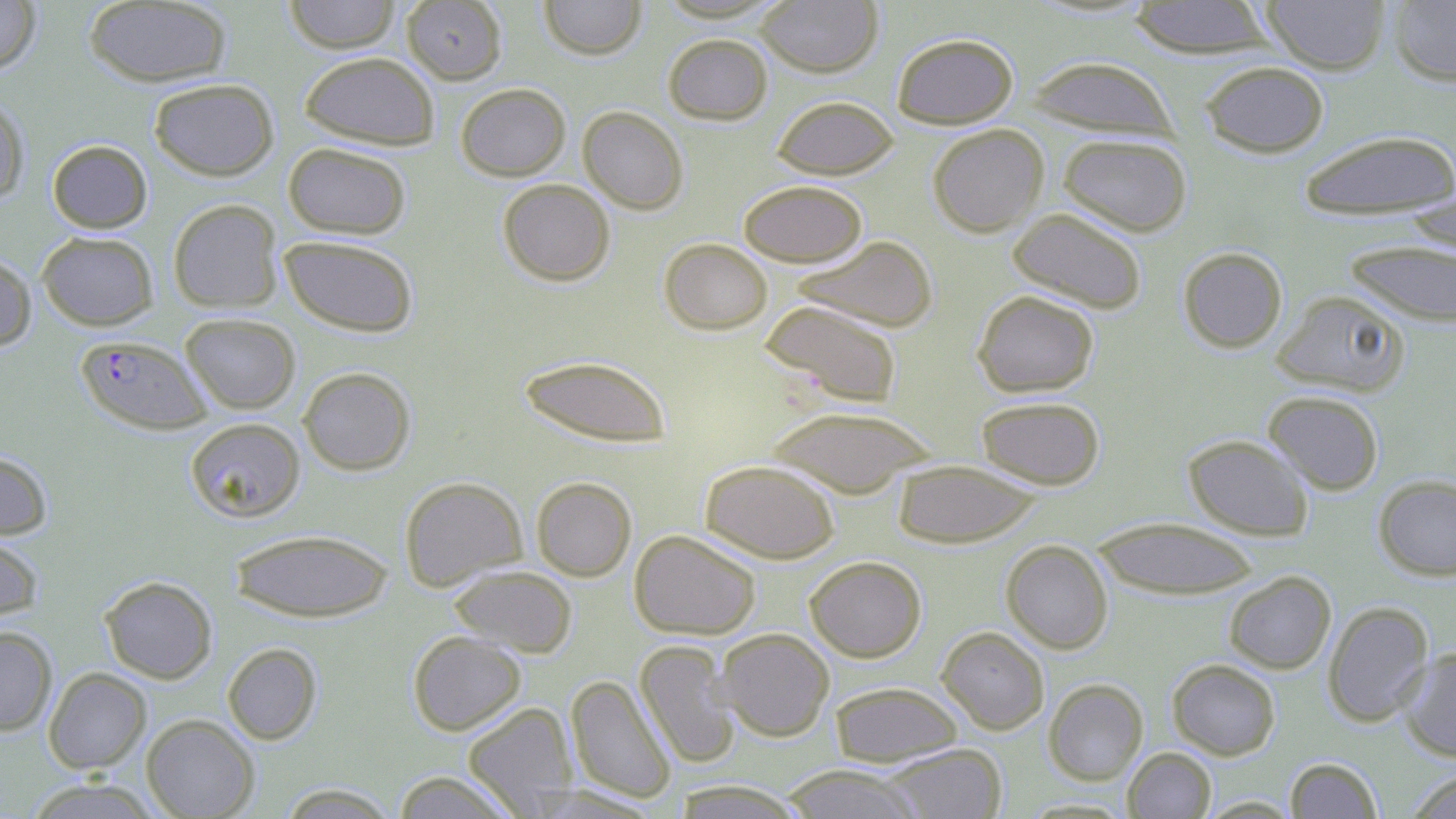
slide-level diagnosis = Plasmodium falciparum
stain = May-Grünwald-Giemsa
image size = 1456×819 pixels
field of view = single
preparation = thin blood film
uninfected red blood cell locations = approximate bounding boxes as (x1,y1)-(x2,y2) corner pairs in pixels: (283,0)-(401,52), (402,0)-(507,84), (539,0)-(646,60), (755,0)-(883,77), (1260,0)-(1391,74), (0,1)-(41,75), (84,1)-(232,88), (1127,1)-(1278,59), (1387,1)-(1456,87), (891,32)-(1018,129), (662,33)-(773,125), (299,51)-(440,150), (1025,55)-(1179,140), (1199,60)-(1330,158), (148,78)-(279,180), (455,82)-(571,181), (771,95)-(899,179), (0,96)-(30,206), (578,106)-(689,214), (927,124)-(1049,237), (1298,130)-(1456,219), (1057,133)-(1193,236), (47,140)-(152,233), (283,142)-(411,239), (497,179)-(615,286), (738,180)-(867,267), (1402,193)-(1455,257), (167,199)-(283,313), (1008,207)-(1148,314), (37,231)-(159,330), (279,235)-(419,337), (791,235)-(939,333), (659,238)-(773,335), (1344,240)-(1456,328), (1177,246)-(1288,353), (0,254)-(37,351), (972,289)-(1100,397), (1272,289)-(1410,397), (759,300)-(904,408), (180,313)-(301,414), (517,354)-(673,448), (298,366)-(416,475), (1262,390)-(1385,494), (975,395)-(1106,490), (763,405)-(939,498), (185,417)-(306,522), (1182,434)-(1314,540), (0,450)-(53,539), (700,459)-(841,563), (892,459)-(1043,548), (1373,474)-(1456,581), (399,476)-(528,592), (531,476)-(636,581), (1090,516)-(1261,599), (228,528)-(394,622), (629,529)-(761,640), (0,532)-(45,624), (1001,539)-(1114,654), (804,556)-(926,662), (449,565)-(577,657), (1224,570)-(1336,674), (99,575)-(217,684), (1322,601)-(1435,726), (0,626)-(58,736), (936,626)-(1050,735), (715,628)-(835,741), (408,630)-(526,735), (634,640)-(741,769), (222,642)-(322,744), (1397,648)-(1456,761), (1167,659)-(1280,760), (43,667)-(151,774), (565,674)-(676,804), (1043,678)-(1148,785), (829,681)-(963,767), (462,702)-(578,816), (141,714)-(259,818), (881,743)-(1008,819), (1123,747)-(1216,819), (1285,757)-(1383,818), (779,764)-(924,819), (1405,768)-(1456,819), (390,770)-(521,818), (22,778)-(161,819), (673,780)-(807,818), (276,783)-(401,818), (527,785)-(664,817), (1197,796)-(1301,818)
modality = light microscopy
Plasmodium falciparum-infected red blood cell locations = approximate bounding boxes as (x1,y1)-(x2,y2) corner pairs in pixels: (75,334)-(213,434)
magnification = 1000x